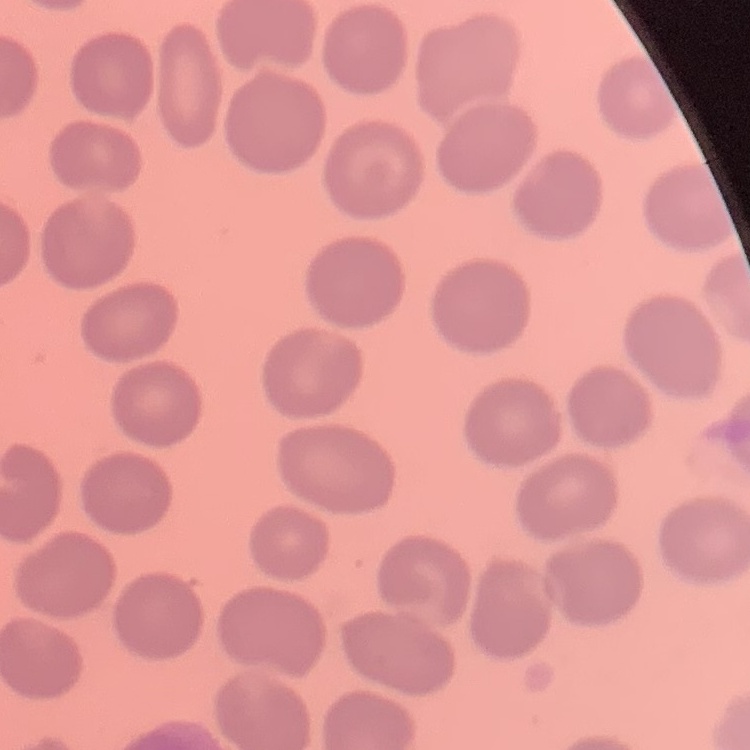
Summary:
  - Red blood cell morphology: no rouleaux formation
  - Preparation: thin blood smear
  - Image type: one tile cut from a larger photomicrograph
  - Stain: Field's or Giemsa